Outline each uninfected red blood cell.
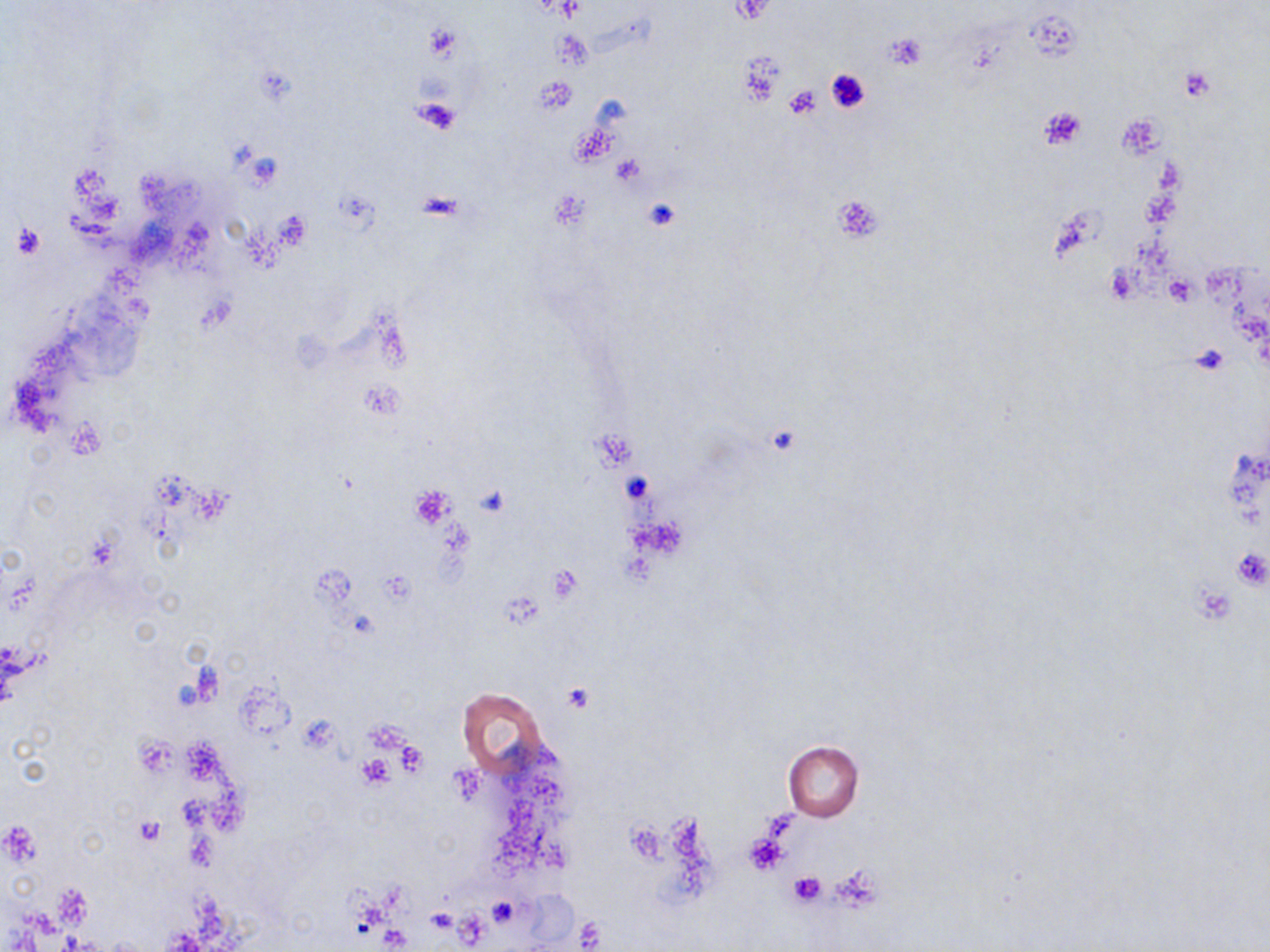

Approximate bounding boxes as (x1,y1)-(x2,y2) corner pairs in pixels.
Uninfected red blood cells: (458,688)-(549,775), (782,741)-(863,821).

slide-level diagnosis = negative for blood parasites
stain = May-Grünwald-Giemsa
image size = 1270×952 pixels
preparation = thin blood film
platelet locations = approximate bounding boxes as (x1,y1)-(x2,y2) corner pairs in pixels: (731,1)-(777,25), (424,26)-(463,60), (887,33)-(927,69), (737,52)-(784,105), (825,67)-(870,113), (1179,68)-(1217,101), (534,75)-(576,114), (782,84)-(823,120), (411,97)-(462,136), (1039,105)-(1086,151), (612,156)-(645,187), (832,194)-(883,244), (644,200)-(680,229), (9,221)-(46,259), (1163,274)-(1198,306), (1190,344)-(1230,376), (411,484)-(455,526), (1230,543)-(1270,591), (545,565)-(583,602), (562,683)-(593,714), (356,755)-(396,789), (450,766)-(483,803), (135,818)-(165,844), (0,822)-(39,868), (744,829)-(787,875), (788,870)-(826,906), (487,896)-(524,927), (426,909)-(456,935), (574,918)-(605,951)
modality = optical microscopy
field of view = one of a larger specimen
magnification = 1000x